Assess this cell for malaria.
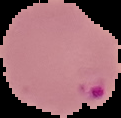

It is parasitized.

Summary:
  - Image type: cell region segmented out of the field of view; surrounding area masked to black
  - Preparation: thin blood smear
  - Image size: 121×118 pixels